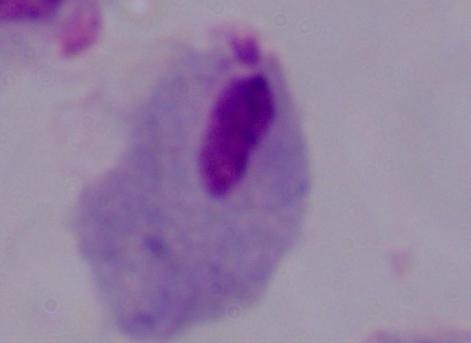
{
  "modality": "micrograph",
  "identification": "trichomonad",
  "magnification": "1000x"
}